Comment on the morphology of the red blood cells.
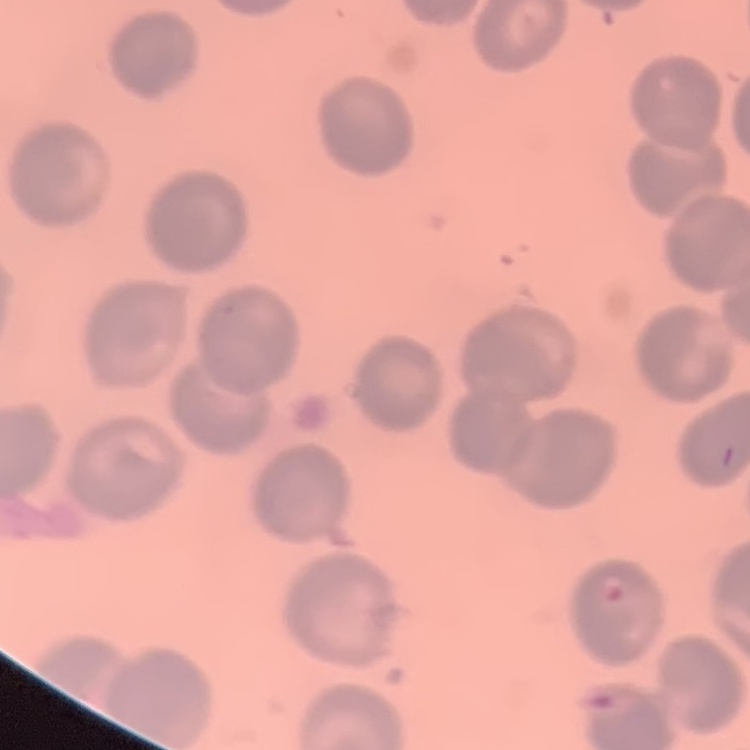
No rouleaux formation.

{
  "stain": "Field's or Giemsa",
  "image_type": "square crop of a larger photomicrograph",
  "preparation": "thin peripheral smear"
}